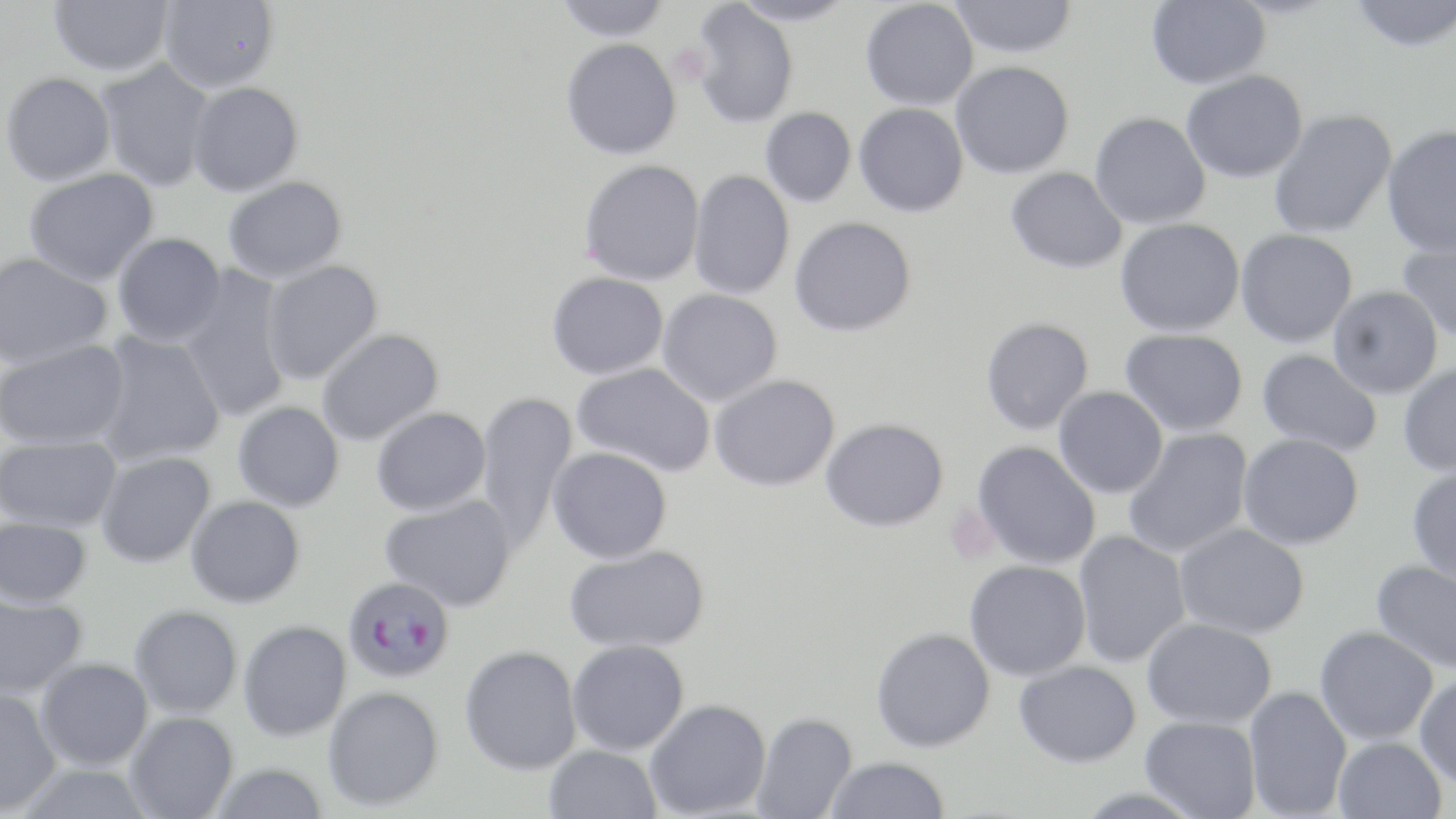

Summary:
  - Coordinate format: approximate bounding boxes as (x1,y1)-(x2,y2) corner pairs in pixels
  - Platelet locations: (667,43)-(711,85)
  - Uninfected red blood cell locations: (49,0)-(173,76), (158,0)-(280,93), (555,0)-(671,42), (730,0)-(854,26), (860,0)-(978,111), (950,0)-(1077,58), (1146,0)-(1270,89), (1349,0)-(1456,53), (690,2)-(798,128), (561,38)-(681,159), (95,59)-(214,192), (951,61)-(1074,179), (1181,70)-(1307,183), (1,72)-(116,186), (188,82)-(304,196), (853,103)-(968,217), (760,108)-(856,208), (1268,108)-(1397,239), (1089,112)-(1210,229), (1381,124)-(1456,256), (579,159)-(704,285), (1005,166)-(1127,273), (23,169)-(159,286), (688,170)-(795,300), (223,177)-(346,283), (789,216)-(916,337), (1115,218)-(1244,337), (1235,228)-(1358,347), (1396,232)-(1456,342), (113,233)-(226,347), (0,252)-(112,369), (262,260)-(383,385), (176,268)-(294,424), (547,272)-(668,379), (1327,285)-(1444,398), (657,289)-(783,406), (980,317)-(1093,434), (316,328)-(443,446), (1120,329)-(1248,436), (91,331)-(225,468), (1,339)-(130,450), (1256,348)-(1382,456), (1397,361)-(1456,477), (572,362)-(716,477), (709,375)-(840,491), (1053,386)-(1168,498), (475,391)-(578,555), (233,401)-(344,512), (371,407)-(490,516), (821,417)-(948,531), (1122,428)-(1255,559), (1238,433)-(1364,550), (0,436)-(122,532), (971,441)-(1101,569), (547,447)-(672,564), (96,452)-(215,568), (1406,466)-(1456,583), (186,495)-(305,608), (380,495)-(517,612), (0,517)-(92,608), (1174,523)-(1310,638), (1072,531)-(1190,667), (564,544)-(709,653), (964,560)-(1090,681), (1371,561)-(1456,673), (0,594)-(88,700), (129,605)-(242,718), (1142,618)-(1277,729), (238,620)-(351,741), (1314,625)-(1438,745), (871,627)-(995,752), (567,639)-(689,754), (459,645)-(582,775), (35,658)-(153,770), (1014,660)-(1141,767), (1414,674)-(1456,787), (1243,685)-(1352,818), (322,686)-(443,811), (0,688)-(62,815), (644,699)-(771,818), (124,711)-(238,819), (752,712)-(858,819), (1140,716)-(1261,819), (1332,737)-(1446,819), (544,745)-(662,819), (824,757)-(950,818), (11,763)-(154,819), (209,763)-(328,819)
  - Plasmodium falciparum-infected red blood cell locations: (343,576)-(454,683)
  - Slide-level diagnosis: Plasmodium falciparum
  - Modality: light microscopy
  - Image size: 1456×819 pixels
  - Preparation: thin blood film
  - Stain: May-Grünwald-Giemsa
  - Field of view: single
  - Magnification: 1000x